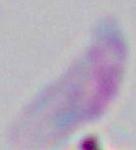
Captured at 1000x magnification. Photomicrograph. Toxoplasma gondii is shown.